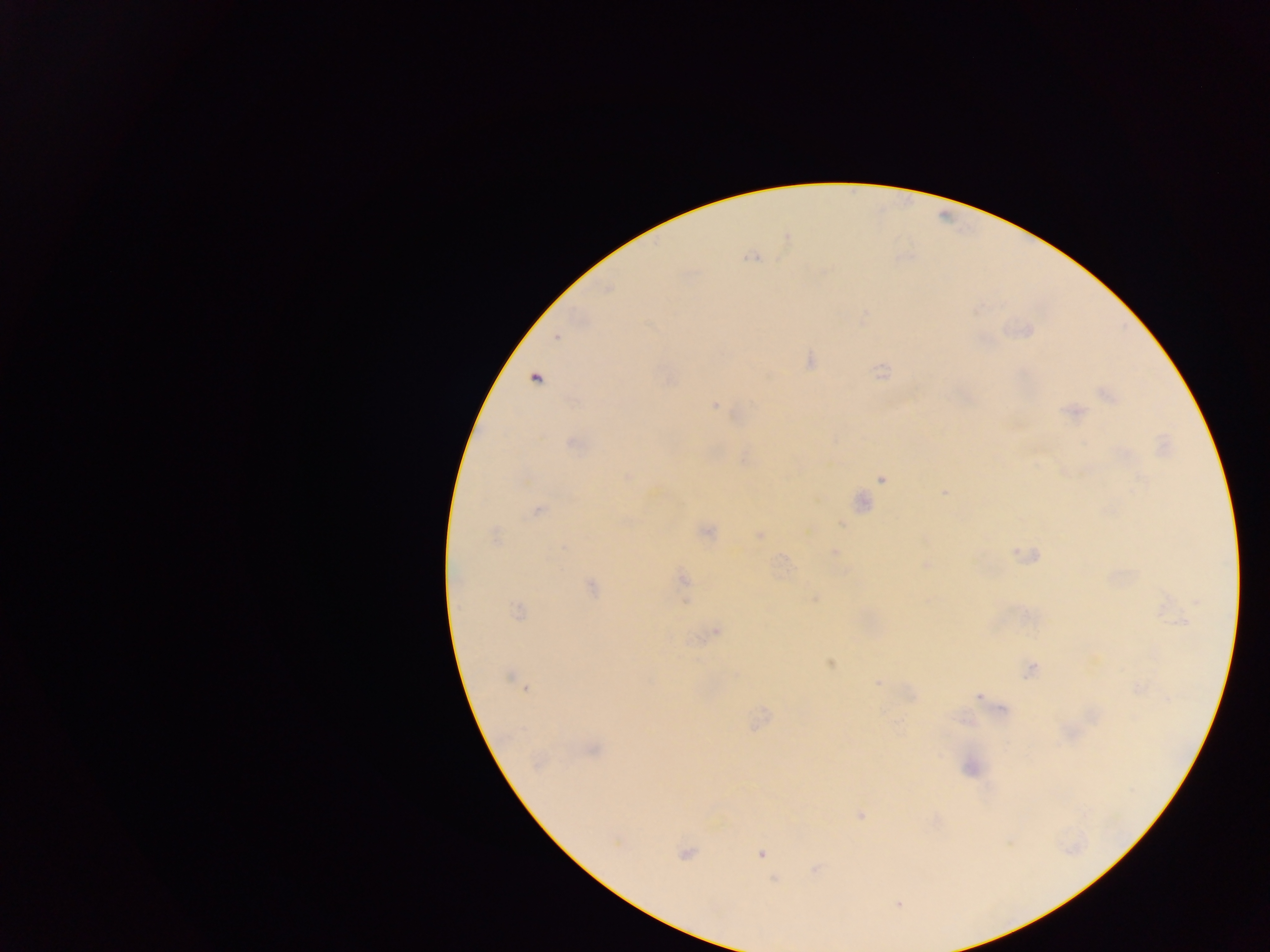

Approximate centers as [x, y] in pixels.
Summary:
  - Malaria parasite locations: [787, 238], [754, 257], [557, 336], [810, 360], [881, 371], [534, 378], [1108, 395], [715, 406], [1074, 411], [571, 442], [626, 476], [883, 477], [944, 492], [860, 502], [537, 510], [705, 531], [758, 535], [494, 536], [834, 552], [1026, 555], [926, 565], [683, 579], [590, 587], [814, 598], [517, 611], [716, 630], [830, 663], [1030, 670], [510, 677], [878, 682], [517, 683], [524, 687], [1137, 687], [979, 695], [1003, 712], [592, 749], [970, 767], [861, 815], [685, 853], [760, 853], [815, 868], [774, 879], [898, 903]
  - Preparation: thick blood smear
  - Capture: mobile-phone photograph through a microscope
  - Country: Ghana
  - Field of view: single
  - Image size: 1270×952 pixels